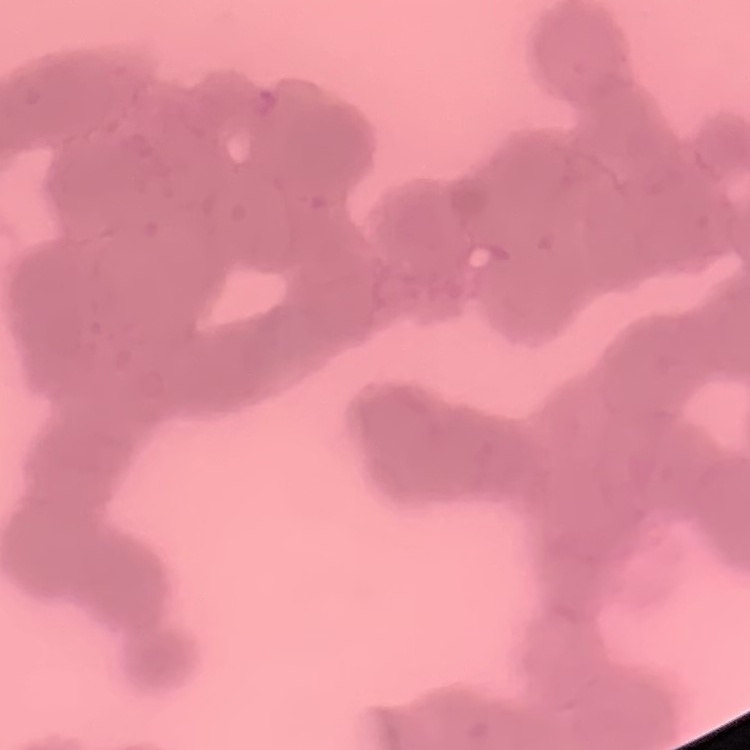

Summary:
  - Erythrocyte morphology: rouleaux formation
  - Stain: Field's or Giemsa
  - Image type: one tile cut from a larger photomicrograph
  - Preparation: thin blood smear